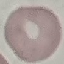

malaria status = uninfected
preparation = thin blood film
image type = cell patch, automatically extracted from a larger field of view and resized to 64 × 64 pixels
stain = Giemsa
capture = smartphone through the microscope eyepiece